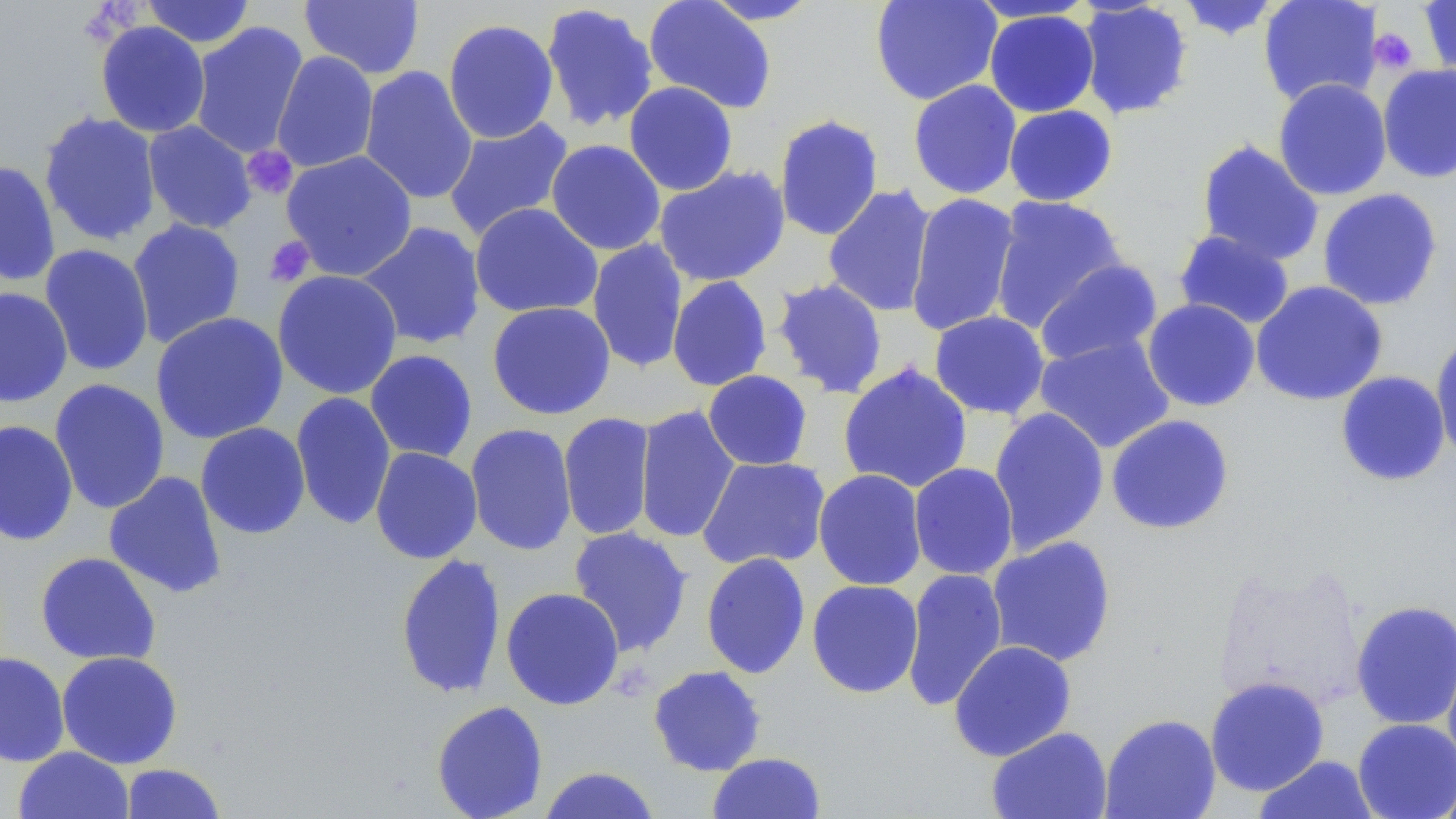
Approximate bounding boxes as (x1, y1, x2, y2) in pixels. Platelet locations: (1368, 28, 1418, 74), (242, 146, 298, 199), (264, 236, 315, 287). Uninfected red blood cell locations: (141, 0, 256, 48), (298, 0, 425, 80), (643, 0, 777, 114), (699, 0, 824, 25), (869, 0, 1002, 106), (1174, 0, 1284, 41), (1258, 0, 1383, 107), (1418, 0, 1456, 81), (966, 1, 1099, 23), (1076, 1, 1194, 120), (539, 2, 659, 133), (984, 9, 1100, 117), (442, 19, 560, 144), (95, 21, 211, 138), (189, 22, 309, 159), (271, 51, 379, 173), (1377, 63, 1456, 184), (358, 66, 478, 205), (1272, 78, 1392, 201), (908, 79, 1023, 199), (623, 81, 738, 195), (1003, 105, 1118, 206), (39, 111, 162, 247), (773, 113, 885, 242), (442, 116, 575, 242), (142, 121, 256, 234), (546, 139, 666, 256), (1196, 139, 1325, 266), (280, 150, 418, 281), (0, 160, 61, 287), (653, 165, 791, 287), (822, 185, 937, 317), (1317, 188, 1443, 311), (905, 192, 1021, 337), (989, 196, 1127, 332), (469, 202, 603, 319), (127, 219, 246, 349), (355, 221, 486, 351), (1173, 229, 1296, 330), (587, 239, 689, 373), (40, 244, 154, 376), (1034, 258, 1163, 369), (272, 270, 403, 400), (667, 276, 773, 392), (771, 278, 888, 398), (1251, 280, 1388, 406), (0, 286, 73, 407), (1142, 299, 1260, 411), (486, 301, 616, 420), (929, 310, 1050, 419), (151, 312, 289, 444), (1430, 333, 1456, 463), (1034, 334, 1175, 454), (364, 349, 478, 463), (837, 363, 973, 494), (703, 370, 813, 471), (1335, 371, 1451, 486), (49, 380, 169, 514), (290, 392, 396, 530), (633, 406, 741, 544), (988, 407, 1110, 554), (558, 412, 656, 541), (1105, 414, 1235, 535), (0, 420, 79, 547), (195, 422, 311, 539), (464, 422, 577, 556), (370, 446, 483, 564), (696, 456, 831, 571), (908, 462, 1019, 580), (813, 469, 927, 591), (104, 471, 228, 599), (568, 526, 693, 657), (987, 536, 1116, 668), (35, 551, 161, 666), (701, 552, 811, 679), (395, 553, 506, 699), (901, 568, 1008, 712), (806, 579, 924, 699), (501, 587, 624, 710), (1350, 599, 1456, 730), (948, 640, 1076, 761), (1442, 642, 1456, 774), (56, 651, 183, 769), (0, 652, 71, 767), (648, 665, 767, 776), (1204, 676, 1330, 796), (431, 700, 548, 819), (1099, 713, 1221, 818), (1352, 718, 1456, 819), (987, 726, 1112, 819), (13, 746, 134, 819), (707, 752, 827, 818), (1252, 754, 1381, 818), (121, 763, 226, 818), (538, 766, 661, 818), (1435, 775, 1456, 819). Slide-level diagnosis: no evidence of blood parasites. Thin blood film. One field of a larger specimen. May-Grünwald-Giemsa stain. Image is 1456×819 pixels. Light microscopy. 1000x magnification.